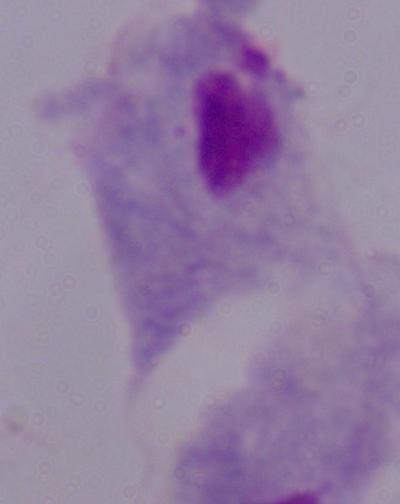

identification = trichomonad
modality = photomicrograph
magnification = 1000x